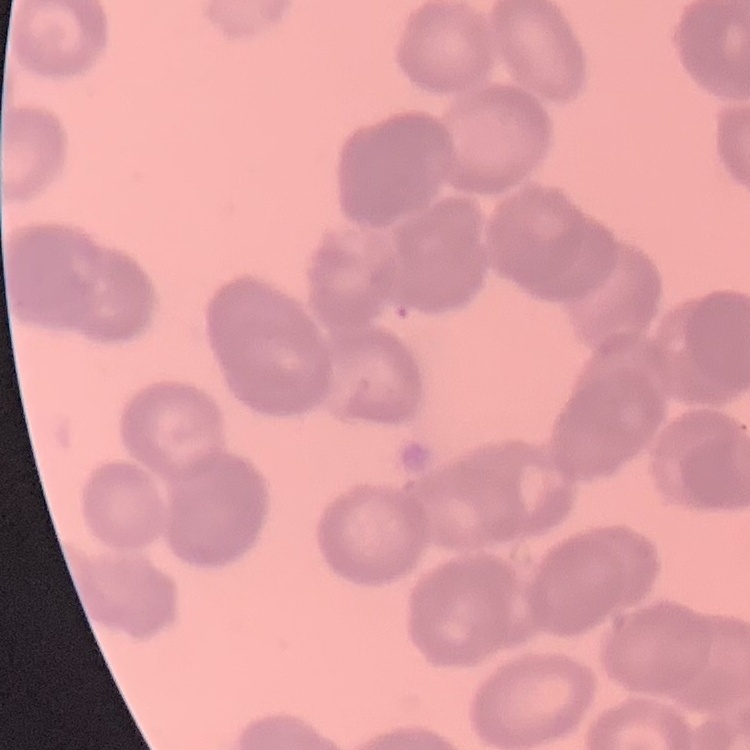

Summary:
  - Red blood cell morphology: rouleaux formation
  - Image type: square crop of a larger photomicrograph
  - Stain: Field's or Giemsa
  - Preparation: thin peripheral smear